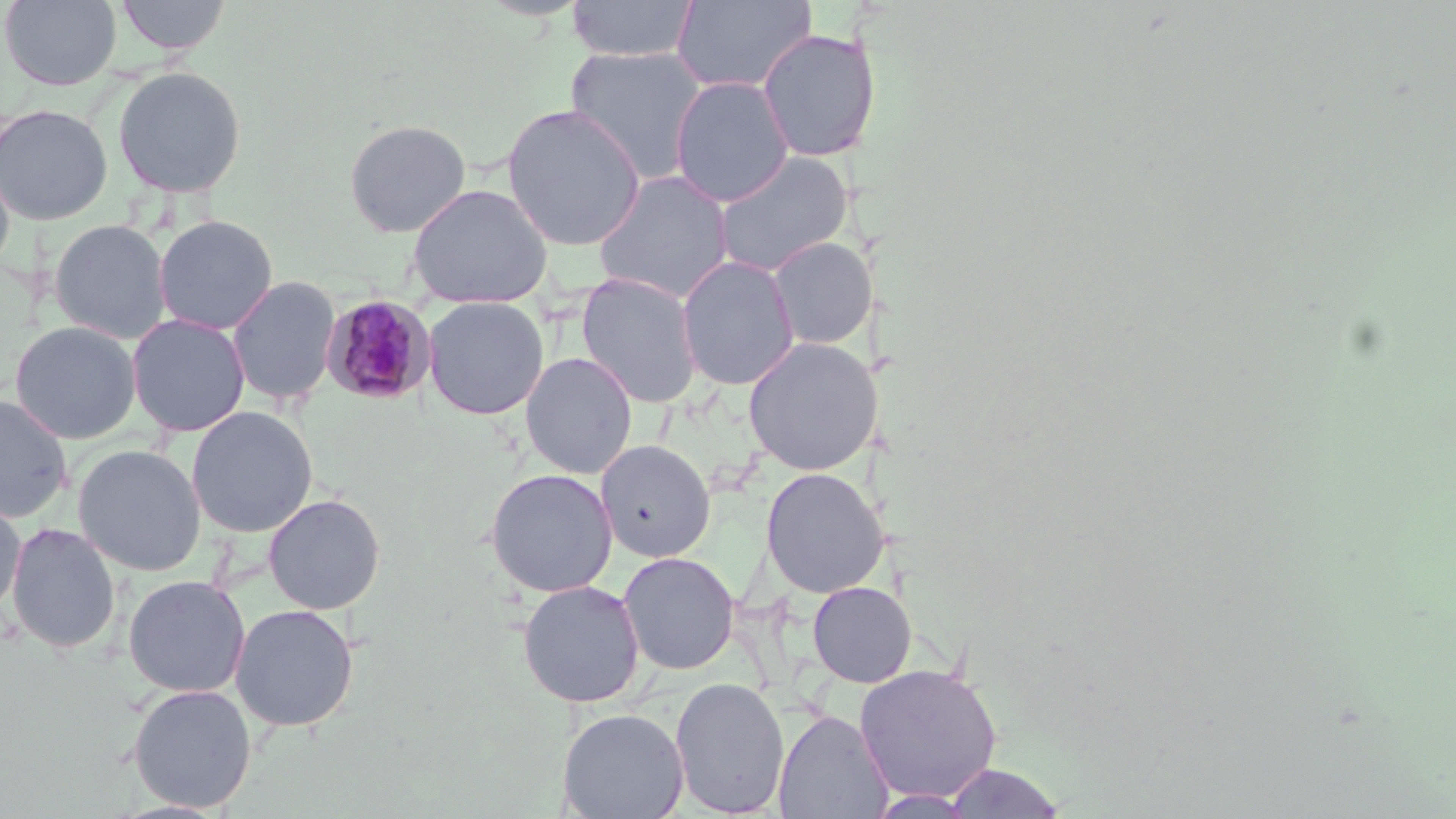

slide-level diagnosis = Plasmodium malariae
uninfected red blood cell locations = approximate bounding boxes as named x1/y1/x2/y2 corners in pixels: (x1=1, y1=0, x2=122, y2=90), (x1=115, y1=0, x2=231, y2=55), (x1=565, y1=0, x2=699, y2=62), (x1=672, y1=0, x2=816, y2=94), (x1=757, y1=29, x2=881, y2=162), (x1=565, y1=45, x2=708, y2=184), (x1=112, y1=65, x2=247, y2=199), (x1=669, y1=76, x2=794, y2=208), (x1=0, y1=103, x2=113, y2=225), (x1=502, y1=103, x2=646, y2=251), (x1=343, y1=118, x2=472, y2=237), (x1=712, y1=150, x2=854, y2=278), (x1=0, y1=158, x2=15, y2=277), (x1=592, y1=170, x2=735, y2=304), (x1=407, y1=183, x2=552, y2=308), (x1=153, y1=214, x2=278, y2=335), (x1=48, y1=219, x2=171, y2=344), (x1=767, y1=236, x2=877, y2=350), (x1=677, y1=255, x2=800, y2=391), (x1=576, y1=272, x2=703, y2=409), (x1=227, y1=275, x2=341, y2=406), (x1=423, y1=296, x2=549, y2=420), (x1=126, y1=313, x2=250, y2=437), (x1=9, y1=321, x2=141, y2=444), (x1=743, y1=337, x2=878, y2=476), (x1=520, y1=352, x2=638, y2=479), (x1=0, y1=394, x2=73, y2=523), (x1=186, y1=406, x2=318, y2=537), (x1=596, y1=440, x2=716, y2=562), (x1=73, y1=444, x2=206, y2=576), (x1=760, y1=467, x2=888, y2=598), (x1=484, y1=468, x2=618, y2=598), (x1=264, y1=494, x2=385, y2=614), (x1=0, y1=495, x2=26, y2=618), (x1=6, y1=522, x2=121, y2=654), (x1=618, y1=551, x2=740, y2=675), (x1=123, y1=574, x2=250, y2=698), (x1=517, y1=580, x2=645, y2=708), (x1=808, y1=581, x2=917, y2=687), (x1=230, y1=603, x2=359, y2=731), (x1=853, y1=663, x2=1003, y2=804), (x1=669, y1=677, x2=790, y2=817), (x1=128, y1=683, x2=257, y2=813), (x1=558, y1=708, x2=689, y2=819), (x1=773, y1=708, x2=893, y2=819), (x1=943, y1=763, x2=1066, y2=818), (x1=867, y1=789, x2=981, y2=817)
modality = optical microscopy
stain = May-Grünwald-Giemsa
magnification = 1000x
field of view = one of a larger specimen
Plasmodium malariae-infected red blood cell locations = approximate bounding boxes as named x1/y1/x2/y2 corners in pixels: (x1=321, y1=294, x2=437, y2=404)
preparation = thin blood smear
image size = 1456×819 pixels